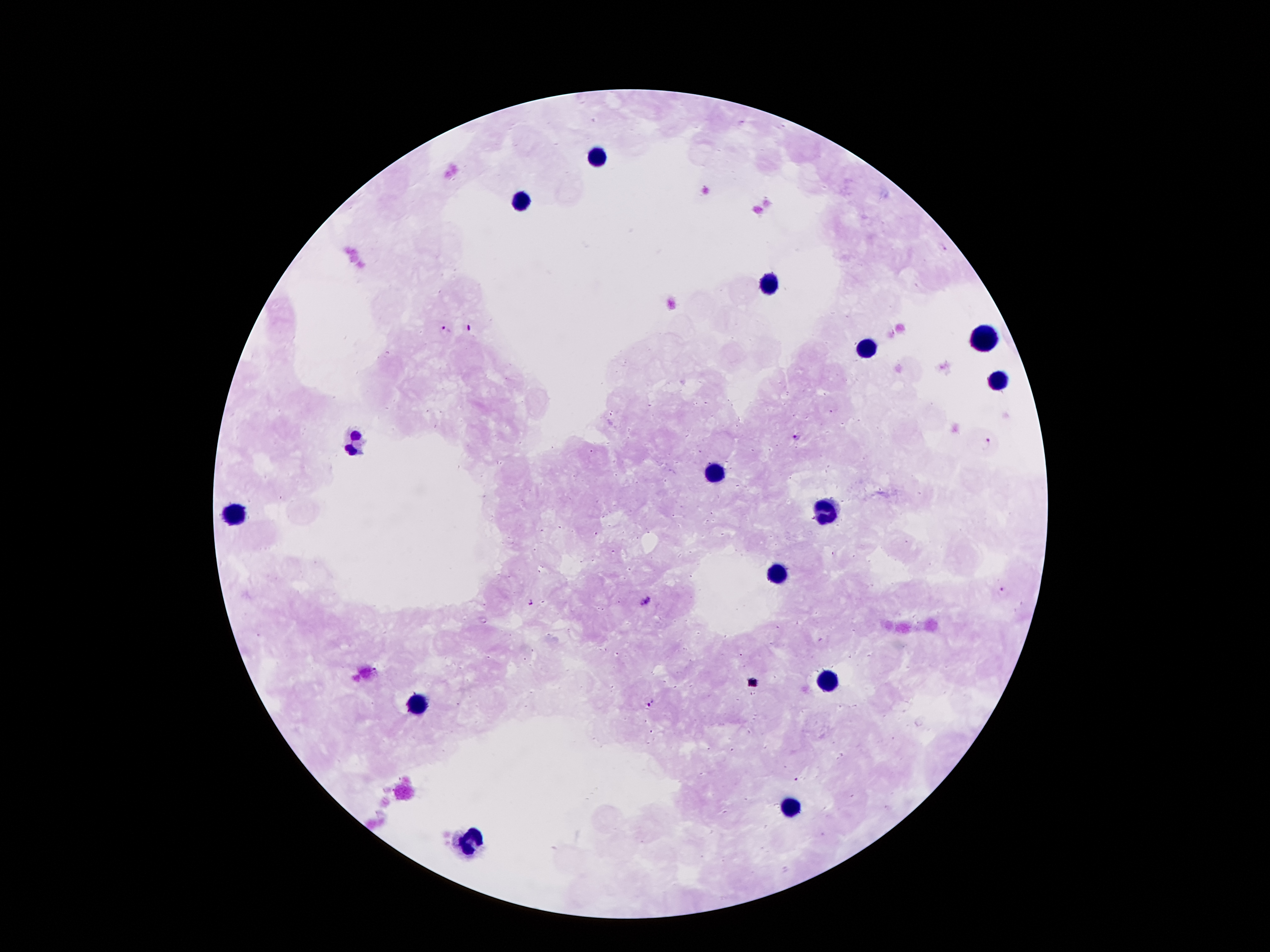
Approximate centers as (x, y) in pixels.
Summary:
  - Leukocyte locations: (597, 155), (523, 202), (767, 283), (985, 339), (863, 348), (993, 382), (357, 440), (712, 473), (828, 510), (232, 515), (779, 577), (824, 681), (413, 706), (789, 809), (470, 844)
  - Malaria parasite locations: (742, 123), (783, 126), (943, 247), (468, 328), (446, 329), (797, 438), (989, 444), (1003, 592), (645, 601), (530, 603), (649, 704)
  - Magnification: 100x
  - Preparation: thick blood smear
  - Field of view: one from this slide
  - Image size: 1270×952 pixels
  - Stain: Giemsa
  - Patient malaria status: positive for Plasmodium falciparum
  - Capture: smartphone through the microscope eyepiece